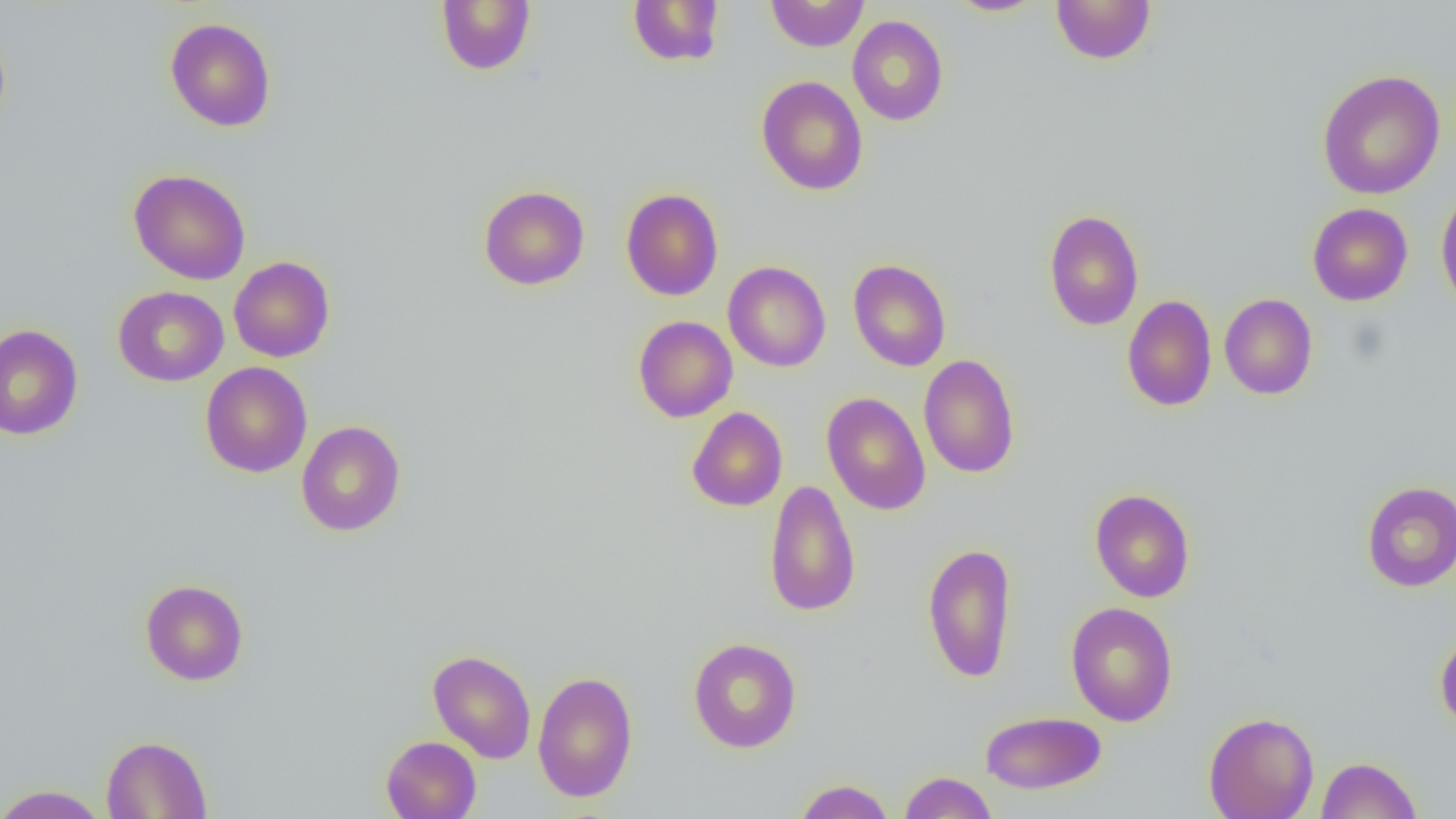
{
  "slide_level_diagnosis": "negative for blood parasites",
  "image_size": "1456×819 pixels",
  "modality": "light microscopy",
  "preparation": "thin blood smear",
  "magnification": "1000x",
  "field_of_view": "single",
  "uninfected_red_blood_cell_locations": "approximate bounding boxes as (x1,y1)-(x2,y2) corner pairs in pixels: (435,0)-(536,75), (627,0)-(726,67), (765,0)-(869,52), (946,0)-(1049,17), (1050,0)-(1157,65), (847,15)-(949,126), (165,17)-(276,132), (1317,69)-(1446,200), (756,75)-(868,196), (128,169)-(251,285), (478,185)-(590,290), (1435,185)-(1456,315), (621,188)-(723,301), (1307,202)-(1413,306), (1043,208)-(1144,331), (229,256)-(335,362), (848,259)-(951,371), (723,261)-(831,372), (113,286)-(228,387), (1219,293)-(1318,400), (1122,294)-(1217,411), (633,315)-(738,422), (0,323)-(83,440), (918,353)-(1020,478), (200,361)-(312,478), (821,391)-(931,515), (686,407)-(787,511), (296,420)-(406,536), (764,479)-(861,617), (1361,481)-(1456,592), (1089,488)-(1195,602), (922,541)-(1018,683), (140,579)-(248,686), (1065,601)-(1178,727), (1435,632)-(1456,734), (688,637)-(801,753), (427,649)-(537,763), (532,670)-(639,802), (980,710)-(1106,794), (1203,711)-(1319,818), (101,735)-(212,818), (381,735)-(481,819), (1316,756)-(1422,818), (898,771)-(998,818), (794,779)-(895,819), (0,784)-(109,818)"
}